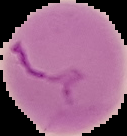

malaria status = parasitized
image type = cell region segmented out of the field of view; surrounding area masked to black
preparation = thin blood smear
image size = 127×136 pixels